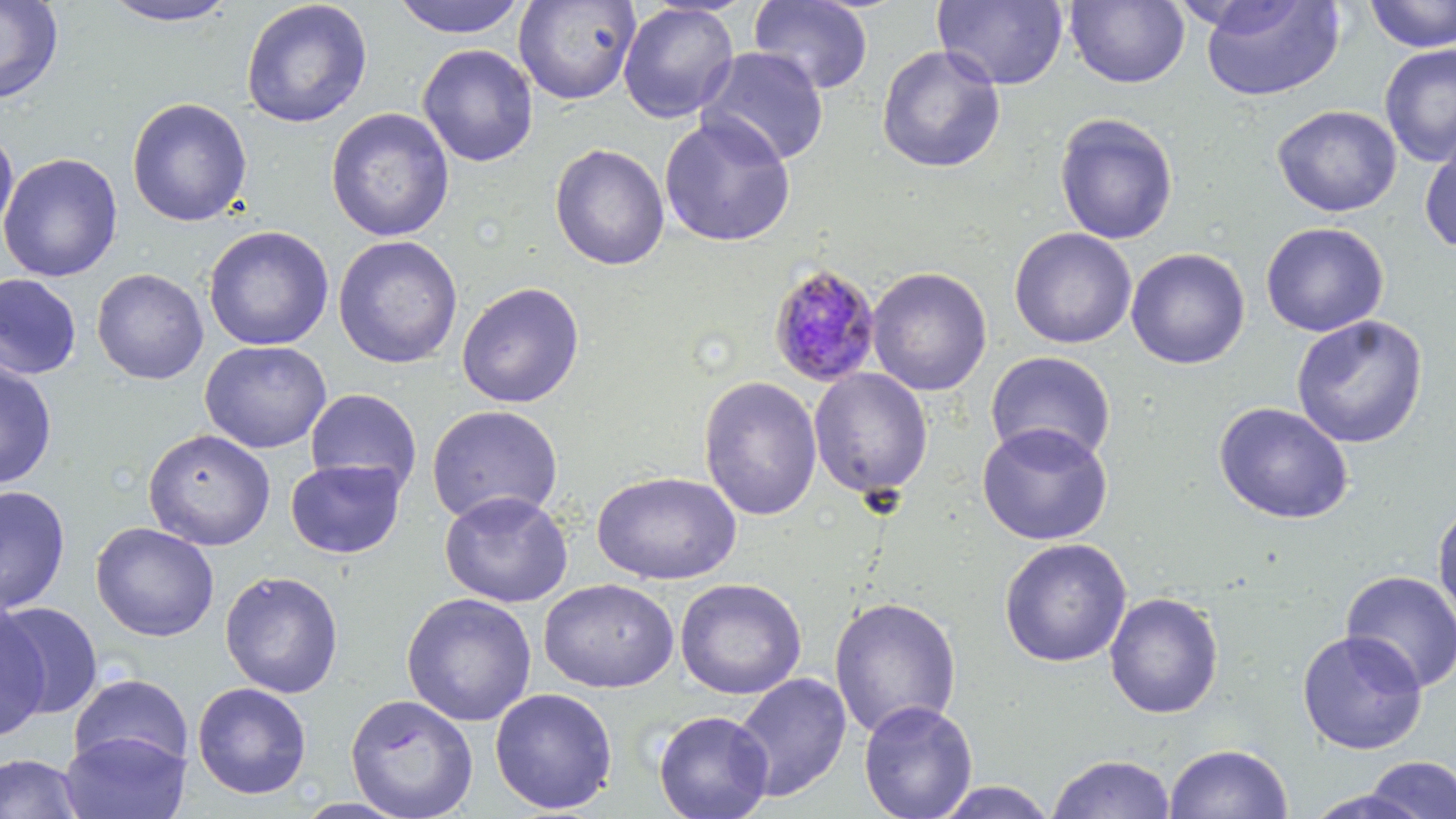

slide-level diagnosis = Plasmodium malariae
modality = light microscopy
stain = May-Grünwald-Giemsa
magnification = 1000x
field of view = one of a larger specimen
preparation = thin blood smear
image size = 1456×819 pixels
uninfected red blood cell locations = approximate bounding boxes as named x1/y1/x2/y2 corners in pixels: (x1=0, y1=0, x2=64, y2=106), (x1=97, y1=0, x2=242, y2=28), (x1=390, y1=0, x2=529, y2=39), (x1=514, y1=0, x2=640, y2=105), (x1=932, y1=0, x2=1069, y2=91), (x1=1199, y1=0, x2=1345, y2=102), (x1=1364, y1=0, x2=1456, y2=53), (x1=240, y1=1, x2=373, y2=129), (x1=748, y1=1, x2=874, y2=95), (x1=1065, y1=1, x2=1190, y2=88), (x1=618, y1=2, x2=740, y2=123), (x1=417, y1=43, x2=539, y2=168), (x1=1378, y1=43, x2=1456, y2=167), (x1=876, y1=44, x2=1007, y2=174), (x1=695, y1=46, x2=830, y2=167), (x1=126, y1=97, x2=253, y2=227), (x1=1272, y1=105, x2=1402, y2=217), (x1=326, y1=107, x2=455, y2=242), (x1=1054, y1=112, x2=1179, y2=245), (x1=659, y1=113, x2=797, y2=247), (x1=0, y1=128, x2=19, y2=244), (x1=1419, y1=136, x2=1456, y2=255), (x1=550, y1=143, x2=670, y2=271), (x1=0, y1=152, x2=123, y2=282), (x1=1260, y1=222, x2=1390, y2=337), (x1=203, y1=225, x2=335, y2=351), (x1=1009, y1=227, x2=1136, y2=349), (x1=333, y1=235, x2=463, y2=369), (x1=1126, y1=248, x2=1250, y2=370), (x1=866, y1=266, x2=993, y2=396), (x1=91, y1=268, x2=209, y2=384), (x1=0, y1=274, x2=81, y2=380), (x1=455, y1=281, x2=586, y2=409), (x1=1291, y1=315, x2=1429, y2=448), (x1=199, y1=340, x2=332, y2=454), (x1=984, y1=351, x2=1117, y2=467), (x1=0, y1=361, x2=58, y2=489), (x1=809, y1=368, x2=933, y2=499), (x1=698, y1=375, x2=822, y2=521), (x1=305, y1=388, x2=421, y2=493), (x1=1213, y1=401, x2=1355, y2=524), (x1=425, y1=404, x2=563, y2=526), (x1=976, y1=422, x2=1113, y2=545), (x1=143, y1=428, x2=276, y2=551), (x1=285, y1=458, x2=407, y2=559), (x1=591, y1=471, x2=742, y2=585), (x1=0, y1=485, x2=71, y2=615), (x1=438, y1=490, x2=574, y2=608), (x1=1432, y1=500, x2=1456, y2=630), (x1=91, y1=521, x2=219, y2=641), (x1=998, y1=537, x2=1132, y2=668), (x1=1340, y1=569, x2=1456, y2=693), (x1=220, y1=570, x2=344, y2=698), (x1=539, y1=578, x2=679, y2=693), (x1=674, y1=578, x2=807, y2=700), (x1=1104, y1=591, x2=1223, y2=719), (x1=401, y1=592, x2=537, y2=727), (x1=828, y1=596, x2=962, y2=739), (x1=1, y1=601, x2=103, y2=719), (x1=0, y1=604, x2=50, y2=741), (x1=1296, y1=630, x2=1427, y2=755), (x1=68, y1=672, x2=193, y2=774), (x1=732, y1=672, x2=852, y2=802), (x1=192, y1=682, x2=312, y2=799), (x1=489, y1=687, x2=618, y2=815), (x1=345, y1=693, x2=478, y2=818), (x1=858, y1=699, x2=978, y2=819), (x1=653, y1=710, x2=774, y2=819), (x1=59, y1=730, x2=191, y2=818), (x1=1164, y1=743, x2=1293, y2=819), (x1=0, y1=753, x2=86, y2=818), (x1=1047, y1=753, x2=1175, y2=819), (x1=1363, y1=756, x2=1456, y2=818), (x1=927, y1=781, x2=1061, y2=818), (x1=1300, y1=788, x2=1433, y2=819)
Plasmodium malariae-infected red blood cell locations = approximate bounding boxes as named x1/y1/x2/y2 corners in pixels: (x1=767, y1=262, x2=882, y2=387)